State the blood parasite species.
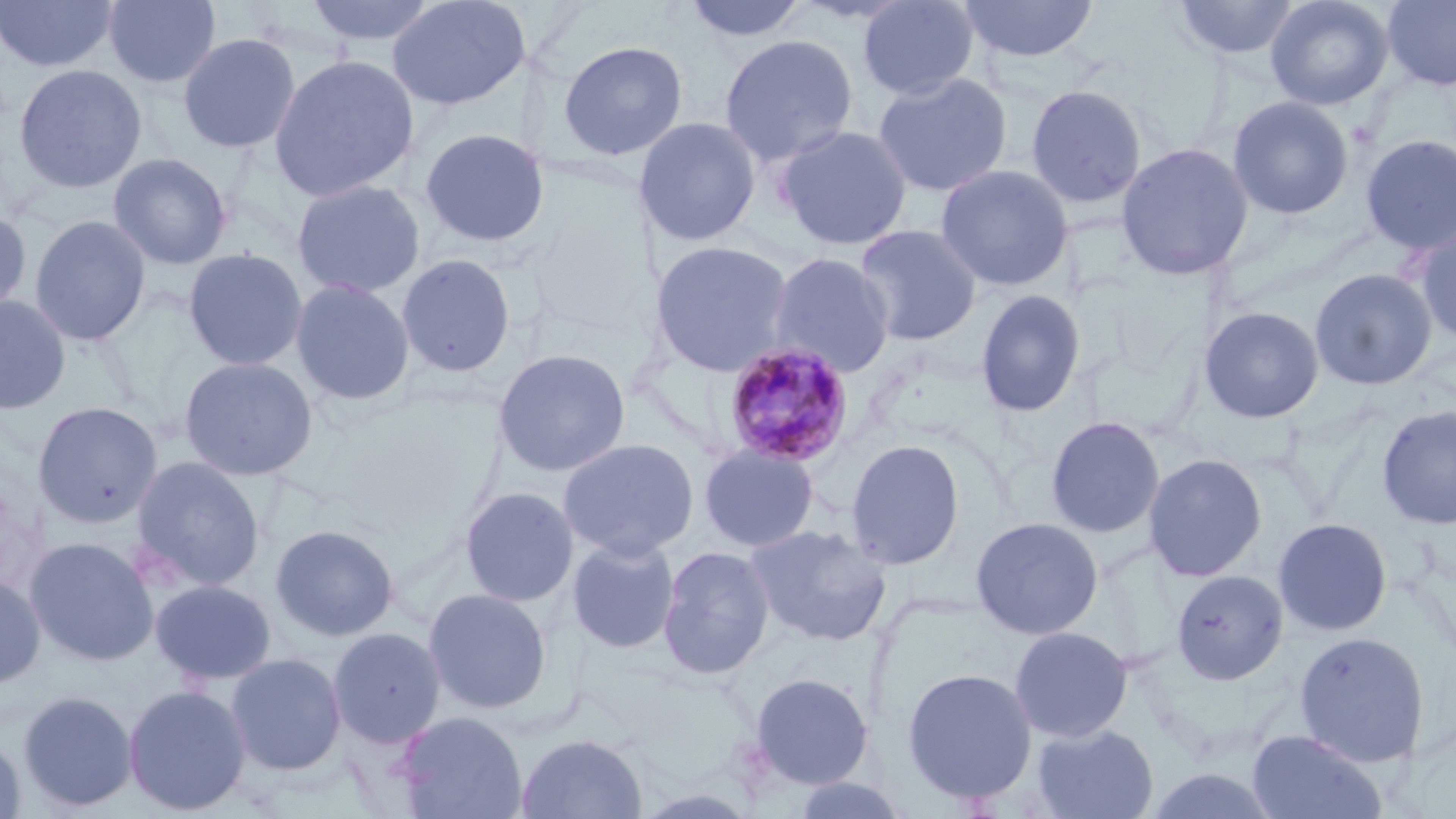

Plasmodium malariae.

stain = May-Grünwald-Giemsa
uninfected red blood cell locations = approximate bounding boxes as [x1, y1, x2, y2] in pixels: [0, 0, 118, 73], [103, 0, 221, 89], [303, 0, 442, 48], [386, 0, 530, 111], [681, 0, 811, 44], [856, 0, 980, 101], [959, 0, 1100, 64], [1172, 0, 1301, 63], [1265, 0, 1394, 111], [1381, 0, 1456, 90], [177, 32, 301, 154], [718, 33, 860, 165], [558, 40, 687, 161], [269, 54, 420, 202], [13, 63, 147, 194], [872, 72, 1013, 197], [1025, 84, 1148, 209], [1227, 95, 1353, 219], [633, 116, 761, 247], [775, 124, 913, 251], [419, 128, 551, 248], [1359, 134, 1456, 255], [1115, 142, 1253, 280], [107, 152, 232, 270], [935, 164, 1074, 291], [291, 179, 426, 299], [0, 208, 31, 318], [29, 214, 151, 346], [1413, 223, 1456, 346], [854, 224, 983, 346], [650, 239, 795, 377], [183, 248, 308, 371], [767, 251, 897, 378], [396, 253, 516, 378], [1309, 268, 1437, 390], [291, 277, 415, 406], [975, 288, 1086, 418], [0, 295, 71, 414], [1198, 305, 1324, 423], [492, 348, 631, 477], [179, 356, 319, 481], [32, 402, 162, 528], [1377, 405, 1456, 530], [1045, 416, 1165, 538], [558, 438, 699, 560], [845, 438, 966, 570], [699, 443, 819, 552], [1143, 453, 1267, 582], [130, 456, 266, 592], [459, 486, 579, 607], [970, 516, 1104, 639], [1273, 517, 1392, 636], [270, 523, 399, 642], [745, 523, 892, 648], [24, 536, 159, 666], [566, 536, 681, 654], [657, 546, 776, 680], [1171, 569, 1288, 685], [0, 573, 46, 691], [149, 579, 277, 686], [423, 587, 552, 715], [1009, 625, 1133, 742], [328, 627, 446, 748], [1294, 631, 1429, 766], [226, 652, 347, 776], [901, 666, 1038, 805], [747, 672, 874, 789], [123, 683, 251, 816], [17, 689, 139, 813], [394, 711, 528, 819], [1031, 723, 1159, 819], [1247, 729, 1386, 819], [515, 732, 648, 818], [0, 733, 26, 819], [1141, 765, 1284, 819], [789, 774, 912, 819]
modality = optical microscopy
magnification = 1000x
Plasmodium malariae-infected red blood cell locations = approximate bounding boxes as [x1, y1, x2, y2] in pixels: [722, 342, 855, 469]
field of view = one of a larger specimen
image size = 1456×819 pixels
preparation = thin blood smear